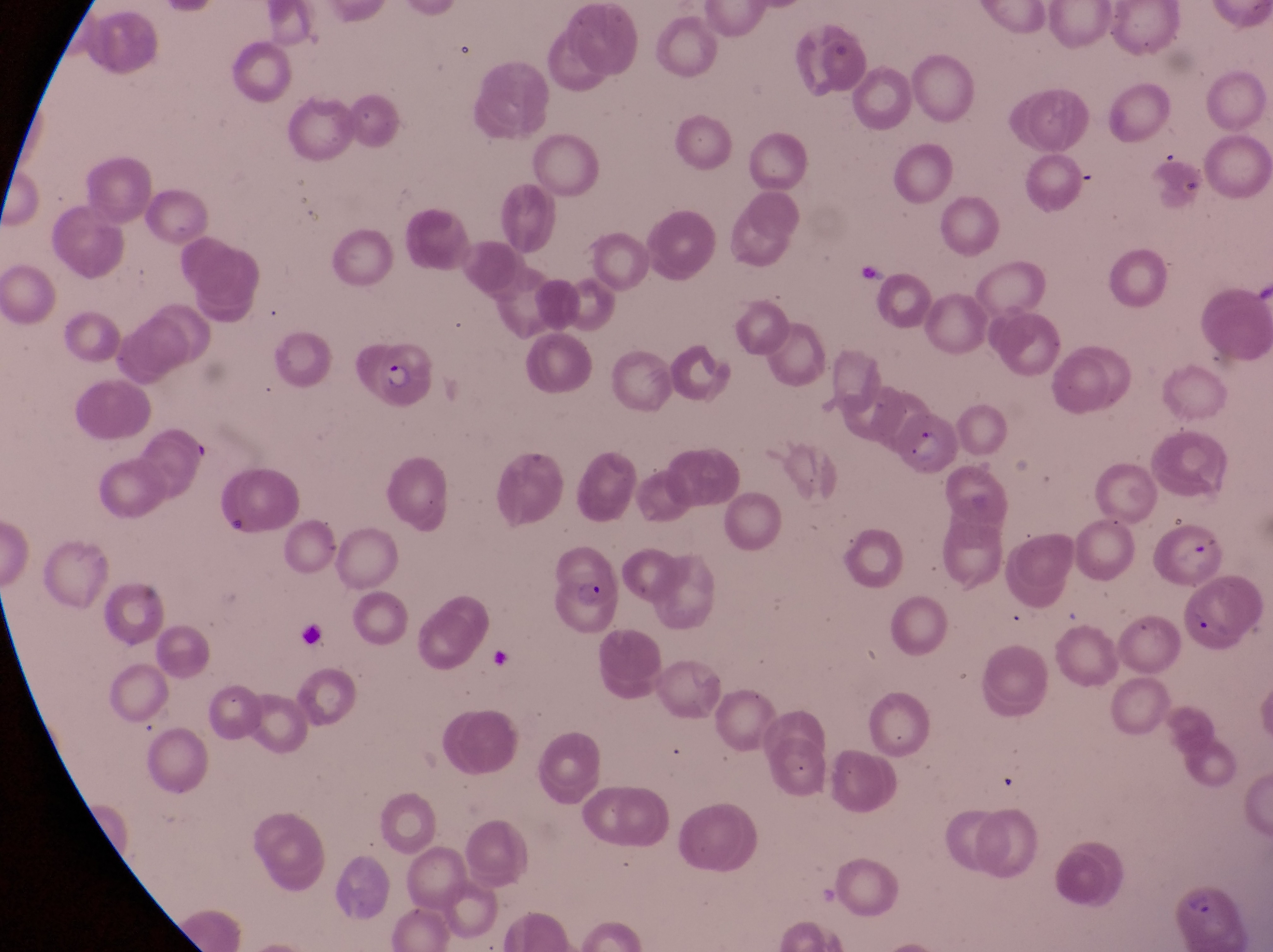
field_of_view: single
image_size: 1273×952 pixels
preparation: thin blood smear
capture: smartphone photograph through the eyepiece of an Olympus CX-23 microscope
magnification: 1000x
parasitised_red_blood_cell_locations: 'approximate bounding boxes as {left, top, right, bottom} in pixels: {364, 337, 434, 399}, {893, 407, 960, 475}, {552, 557, 617, 631}, {1165, 881, 1242, 948}'
artifact_platelet_like_body_stain_precipitate_or_debris_locations: 'approximate bounding boxes as {left, top, right, bottom} in pixels: {218, 509, 258, 542}, {1185, 534, 1213, 566}, {1186, 604, 1239, 641}, {289, 619, 332, 658}'
country: Uganda